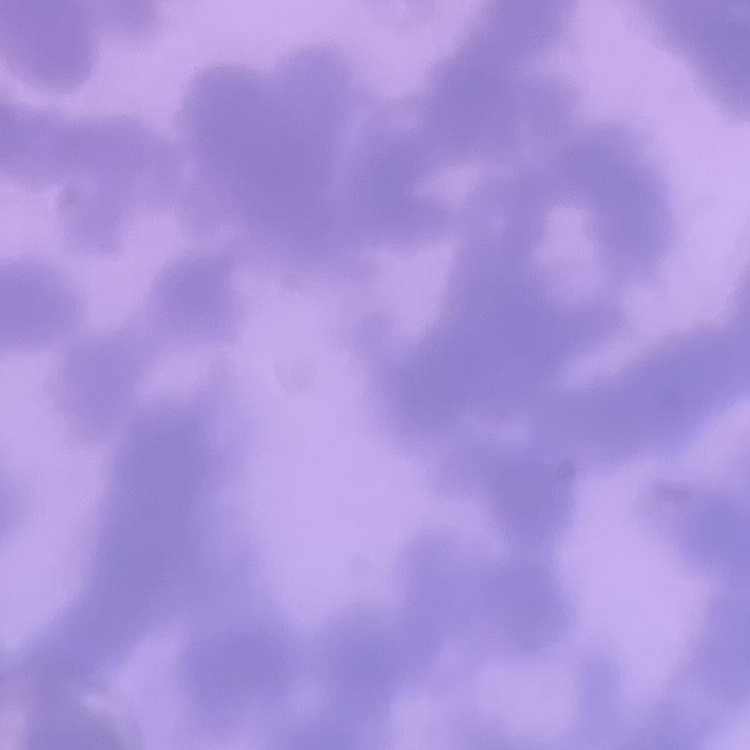
Summary:
  - Red blood cell morphology: rouleaux formation
  - Preparation: thin blood film
  - Image type: square crop of a larger photomicrograph
  - Stain: Field's or Giemsa